Classify this cell by malaria status.
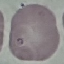

It is uninfected.

Summary:
  - Preparation: thin smear
  - Capture: smartphone camera at the microscope eyepiece
  - Image type: automatically extracted cell patch, resized to 64 × 64 pixels
  - Stain: Giemsa